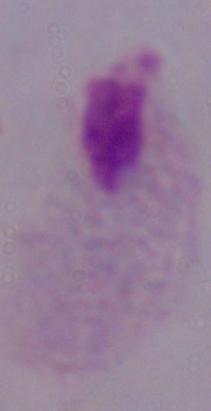
identification = trichomonad
magnification = 1000x
modality = photomicrograph